Report the malaria status of this cell.
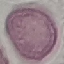

It is uninfected.

Summary:
  - Image type: cell patch, automatically extracted from a larger field of view and resized to 64 × 64 pixels
  - Stain: Giemsa
  - Capture: smartphone camera at the microscope eyepiece
  - Preparation: thin smear